Identify the cell.
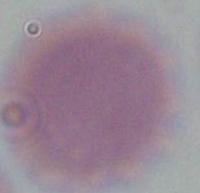
An erythrocyte.

Captured at 1000x magnification. Micrograph.